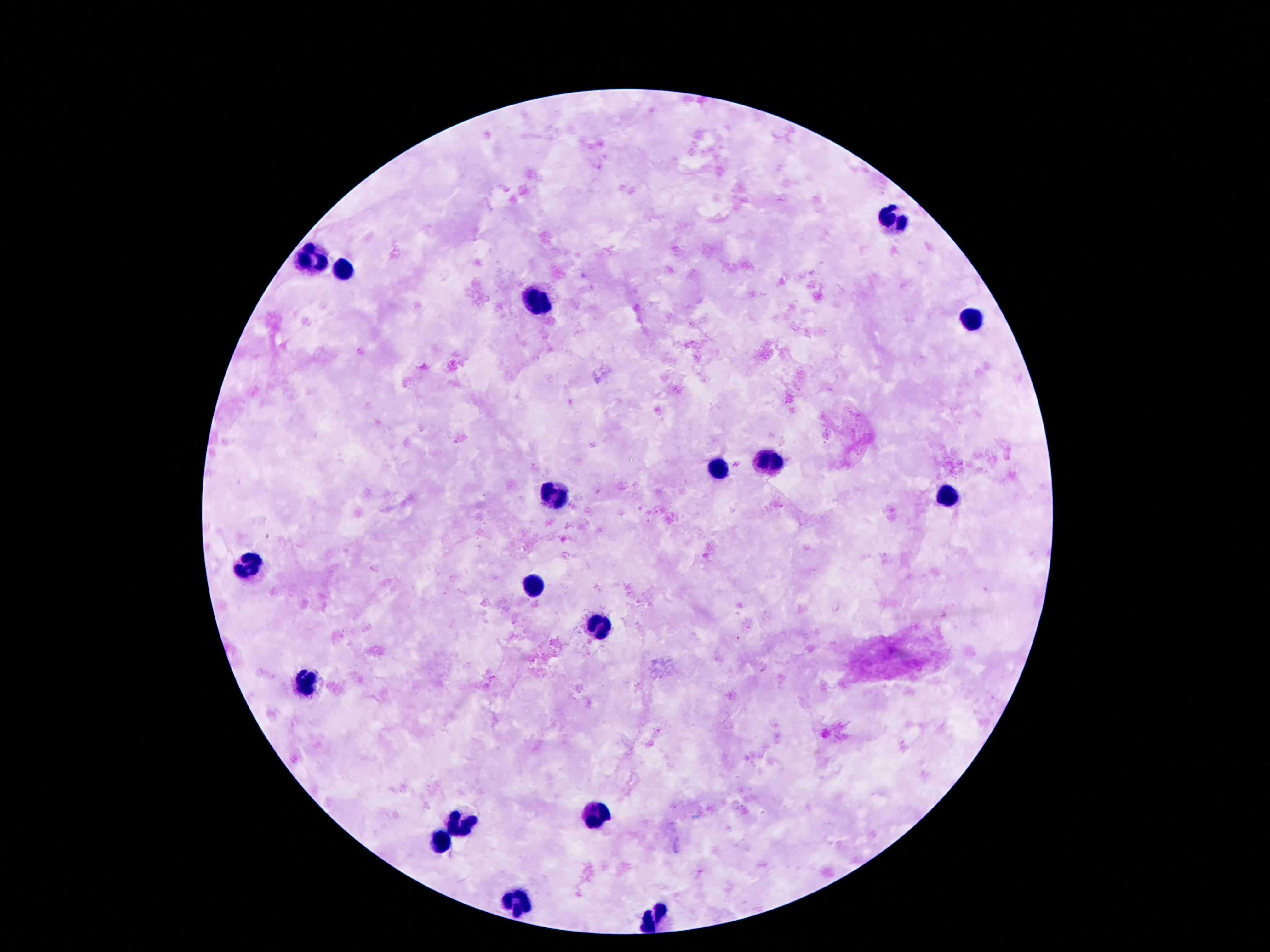

preparation = thick peripheral-blood smear
image size = 1270×952 pixels
magnification = 100x
leukocyte locations = approximate centers as (x, y) in pixels: (891, 222), (314, 260), (344, 272), (539, 299), (973, 319), (766, 459), (714, 469), (950, 496), (553, 498), (255, 567), (535, 585), (603, 624), (307, 682), (596, 814), (460, 826), (439, 842), (514, 907), (650, 923)
capture = smartphone camera through the microscope eyepiece
stain = Giemsa
patient malaria status = negative
field of view = single